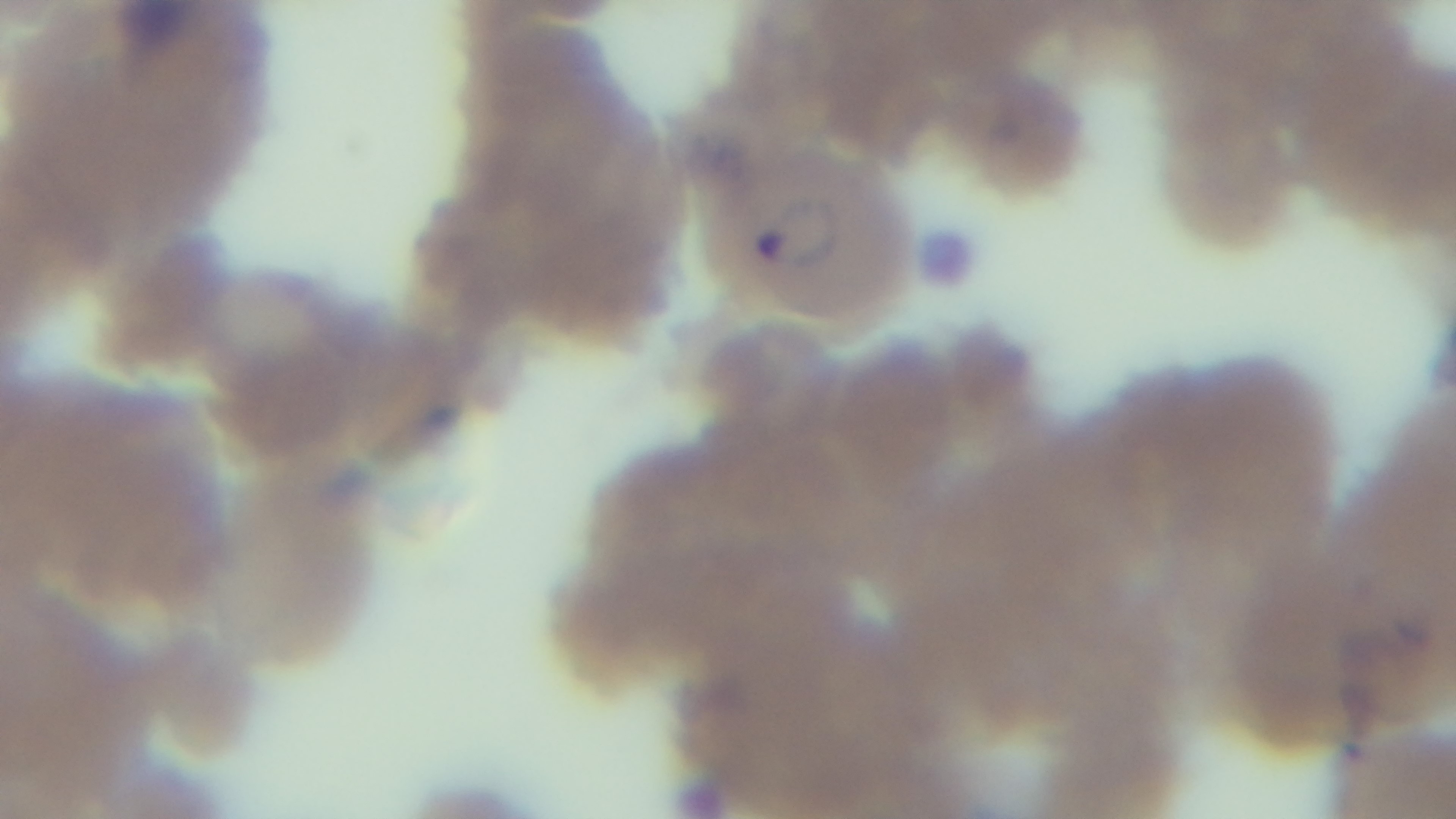

Light microscopy. Preparation: thin. Giemsa-stained. Malaria status: infected. Captured with a mounted 4K digital camera. One field from the slide. 100x oil-immersion objective.